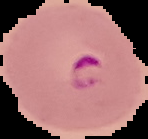

Summary:
  - Image type: cell region segmented out of the field of view; surrounding area masked to black
  - Result: Plasmodium parasites detected
  - Preparation: thin blood film
  - Image size: 148×139 pixels